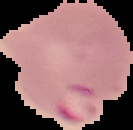
Summary:
  - Image size: 133×130 pixels
  - Image type: cell region segmented out of the field of view; surrounding area masked to black
  - Preparation: thin blood smear
  - Result: malaria parasites identified